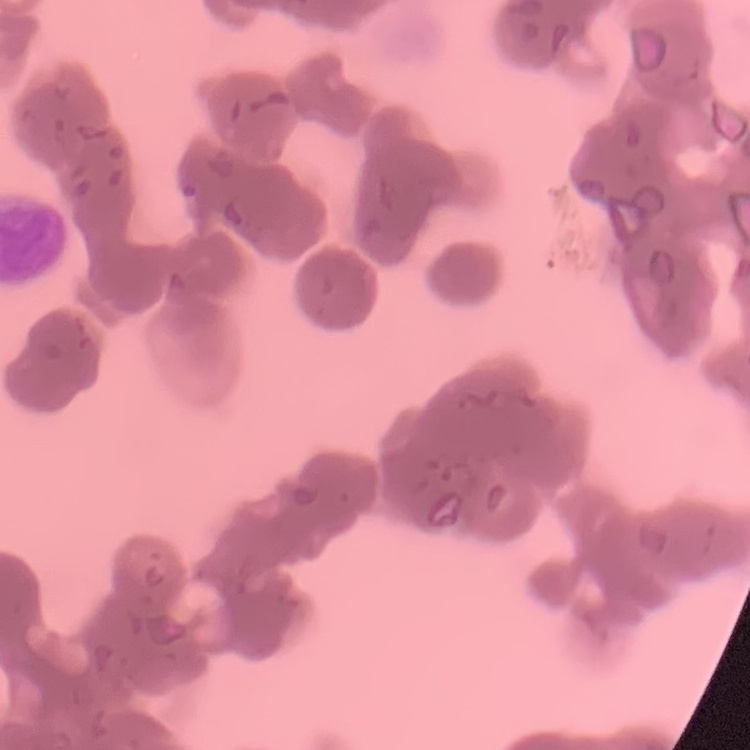
red blood cell morphology = rouleaux formation
image type = square crop of a larger photomicrograph
stain = Field's or Giemsa
preparation = thin peripheral smear